Identify the preparation type.
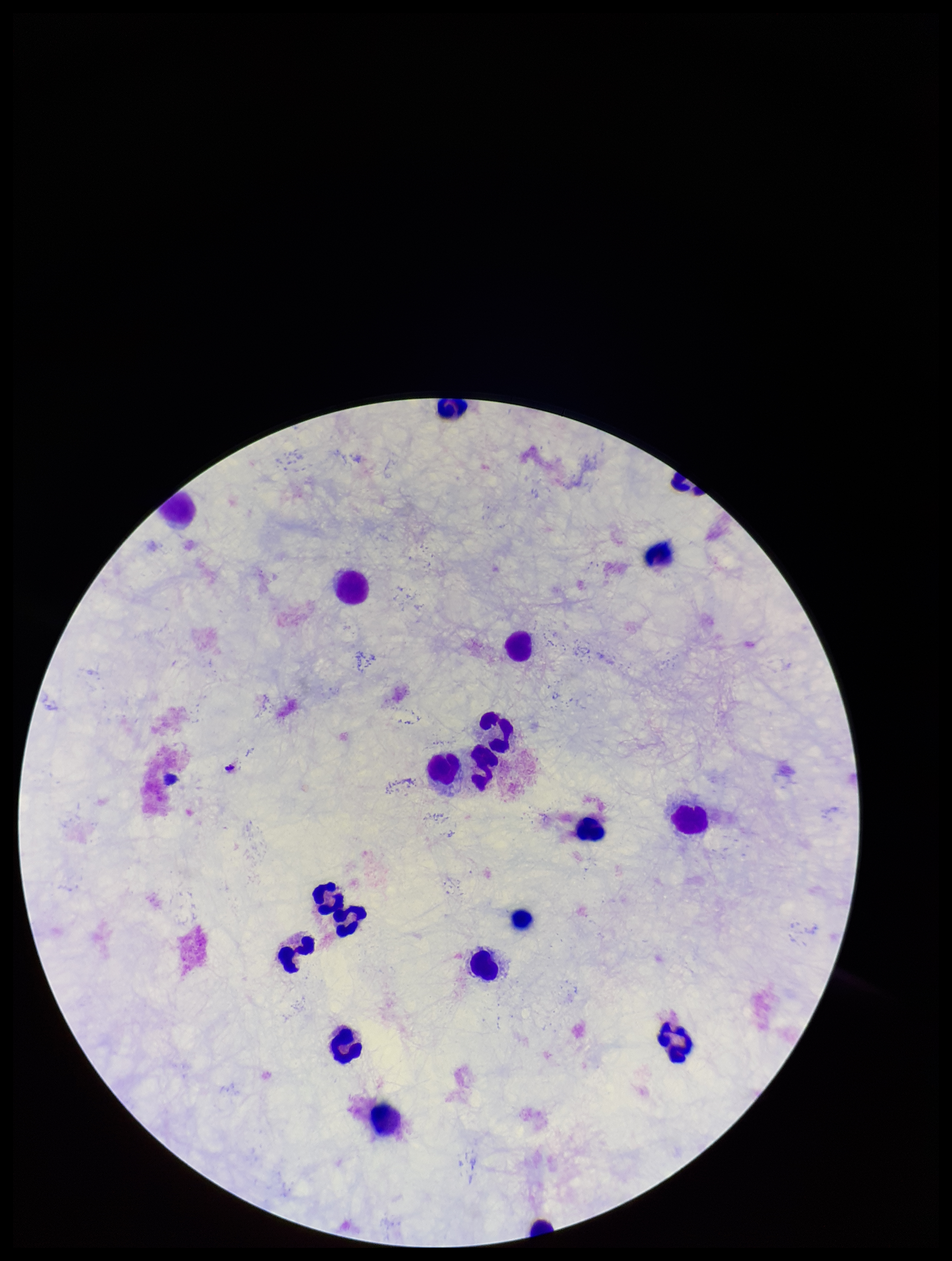
A thick smear.

Photographed through the microscope eyepiece with a smartphone camera. Parasite count: 0. One field from this slide. Plasmodium parasites: none identified. Giemsa stain. Patient malaria status: negative. Image is 952×1261 pixels. Leukocyte count: 18.